Identify the blood parasite species.
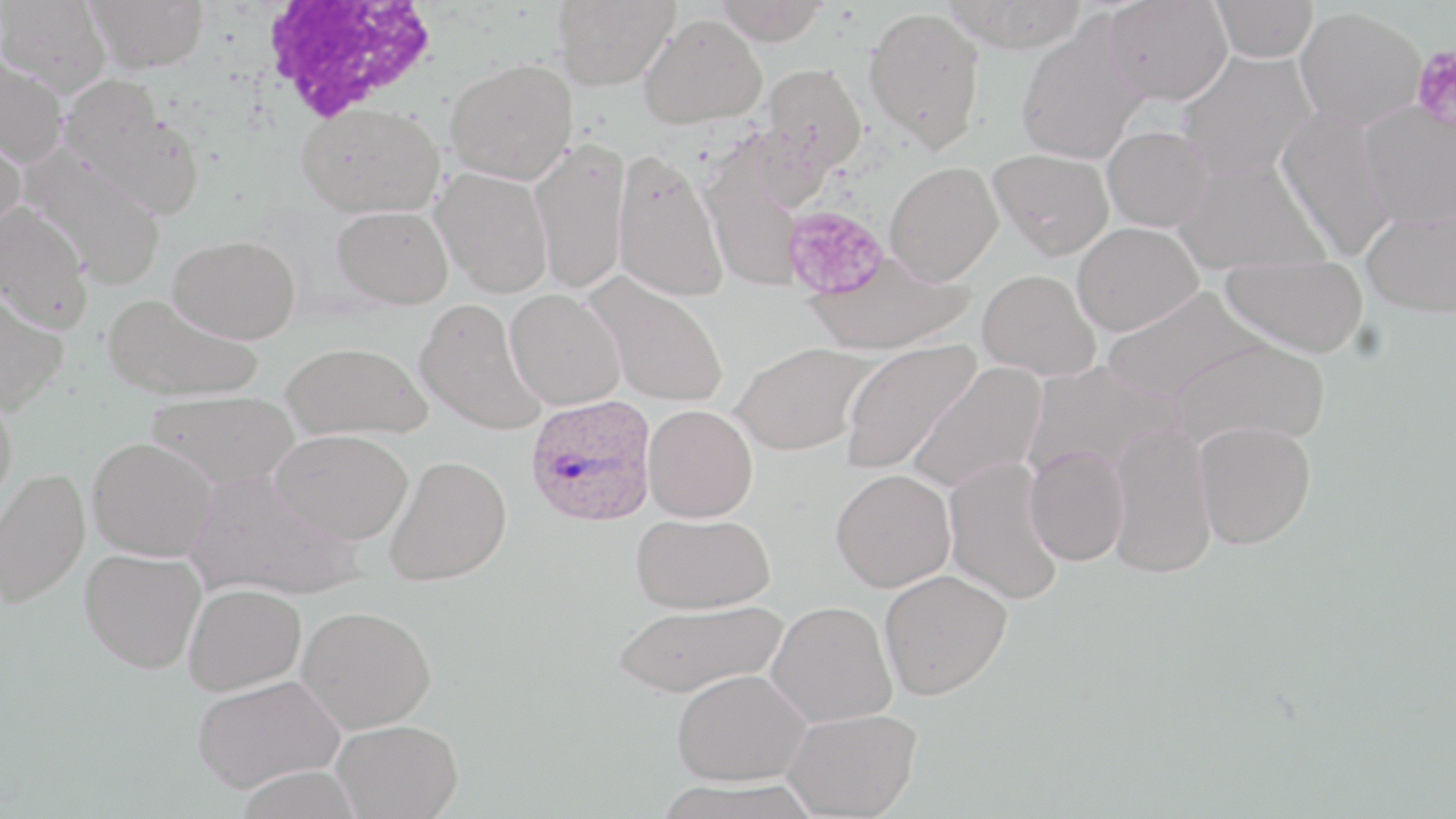

Plasmodium ovale.

{
  "stain": "May-Grünwald-Giemsa",
  "platelet_locations": "approximate bounding boxes as (x1,y1)-(x2,y2) corner pairs in pixels: (1411,44)-(1456,134), (782,205)-(890,301)",
  "magnification": "1000x",
  "modality": "optical microscopy",
  "uninfected_red_blood_cell_locations": "approximate bounding boxes as (x1,y1)-(x2,y2) corner pairs in pixels: (0,0)-(112,97), (84,0)-(209,73), (553,0)-(678,90), (714,0)-(828,45), (941,0)-(1088,52), (1102,0)-(1233,105), (1211,1)-(1318,63), (864,6)-(986,152), (1294,6)-(1426,131), (640,14)-(766,128), (1016,19)-(1150,164), (1177,49)-(1317,182), (0,56)-(68,167), (445,58)-(578,184), (762,63)-(867,174), (57,71)-(176,180), (67,100)-(205,219), (295,101)-(444,219), (1357,102)-(1455,229), (1276,107)-(1398,259), (0,118)-(27,238), (1102,126)-(1213,231), (529,137)-(631,295), (988,147)-(1114,258), (612,148)-(729,303), (700,150)-(808,295), (24,151)-(167,289), (1174,158)-(1327,276), (884,160)-(1004,285), (431,167)-(554,297), (0,202)-(93,334), (1361,204)-(1456,318), (331,205)-(454,308), (1071,222)-(1203,335), (168,233)-(301,343), (804,251)-(972,355), (1221,253)-(1368,357), (977,269)-(1101,381), (585,273)-(729,408), (0,288)-(69,414), (505,288)-(626,410), (1101,288)-(1265,404), (103,294)-(262,402), (413,297)-(545,436), (1170,337)-(1330,449), (840,338)-(980,475), (281,341)-(432,441), (731,342)-(874,456), (1021,359)-(1185,481), (907,361)-(1047,495), (0,390)-(18,515), (147,391)-(301,487), (643,404)-(758,522), (1194,420)-(1316,549), (1107,422)-(1217,578), (270,428)-(414,545), (86,436)-(218,561), (1024,445)-(1129,566), (384,454)-(512,586), (943,457)-(1065,605), (0,468)-(89,608), (831,469)-(956,591), (184,470)-(361,601), (630,512)-(776,614), (79,548)-(206,673), (878,569)-(1012,700), (183,583)-(306,695), (611,599)-(787,699), (766,601)-(897,728), (297,605)-(436,733), (672,669)-(811,786), (192,674)-(344,793), (783,708)-(921,818), (331,718)-(462,818)",
  "field_of_view": "one of a larger specimen",
  "preparation": "thin blood smear",
  "image_size": "1456×819 pixels",
  "plasmodium_ovale_infected_red_blood_cell_locations": "approximate bounding boxes as (x1,y1)-(x2,y2) corner pairs in pixels: (525,394)-(657,527)",
  "white_blood_cell_locations": "approximate bounding boxes as (x1,y1)-(x2,y2) corner pairs in pixels: (258,0)-(438,123)"
}